Locate every Plasmodium parasite.
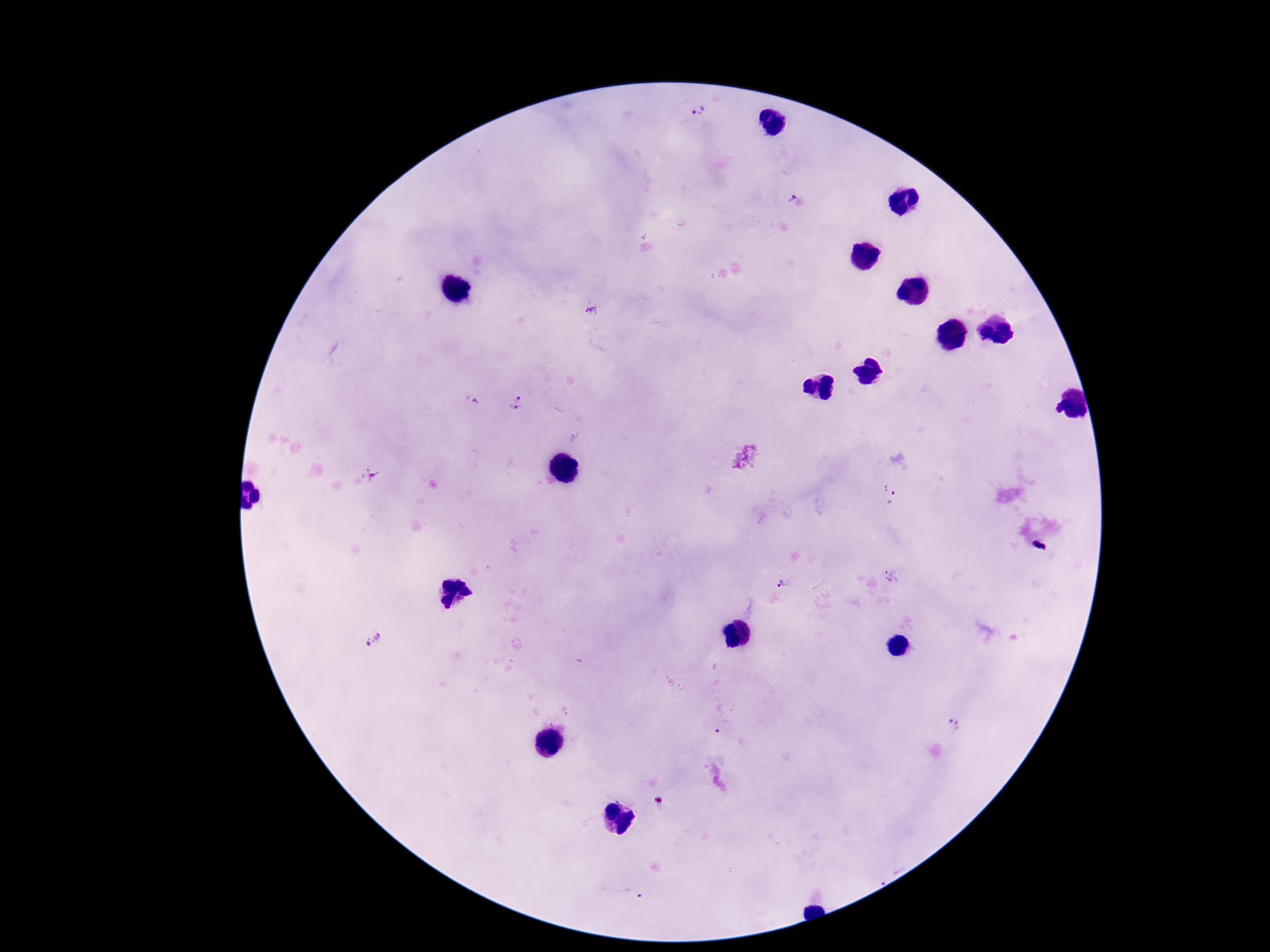
Approximate centers as [x, y] in pixels.
Plasmodium parasites: [698, 112], [794, 201], [592, 310], [518, 398], [475, 401], [516, 408], [371, 474], [884, 487], [893, 499], [891, 576], [782, 584], [373, 637], [954, 725], [722, 727], [632, 895].

Summary:
  - Stain: Giemsa
  - Capture: smartphone camera through the microscope eyepiece
  - Preparation: thick blood smear
  - Field of view: single
  - Magnification: 100x
  - Patient malaria status: positive
  - Image size: 1270×952 pixels